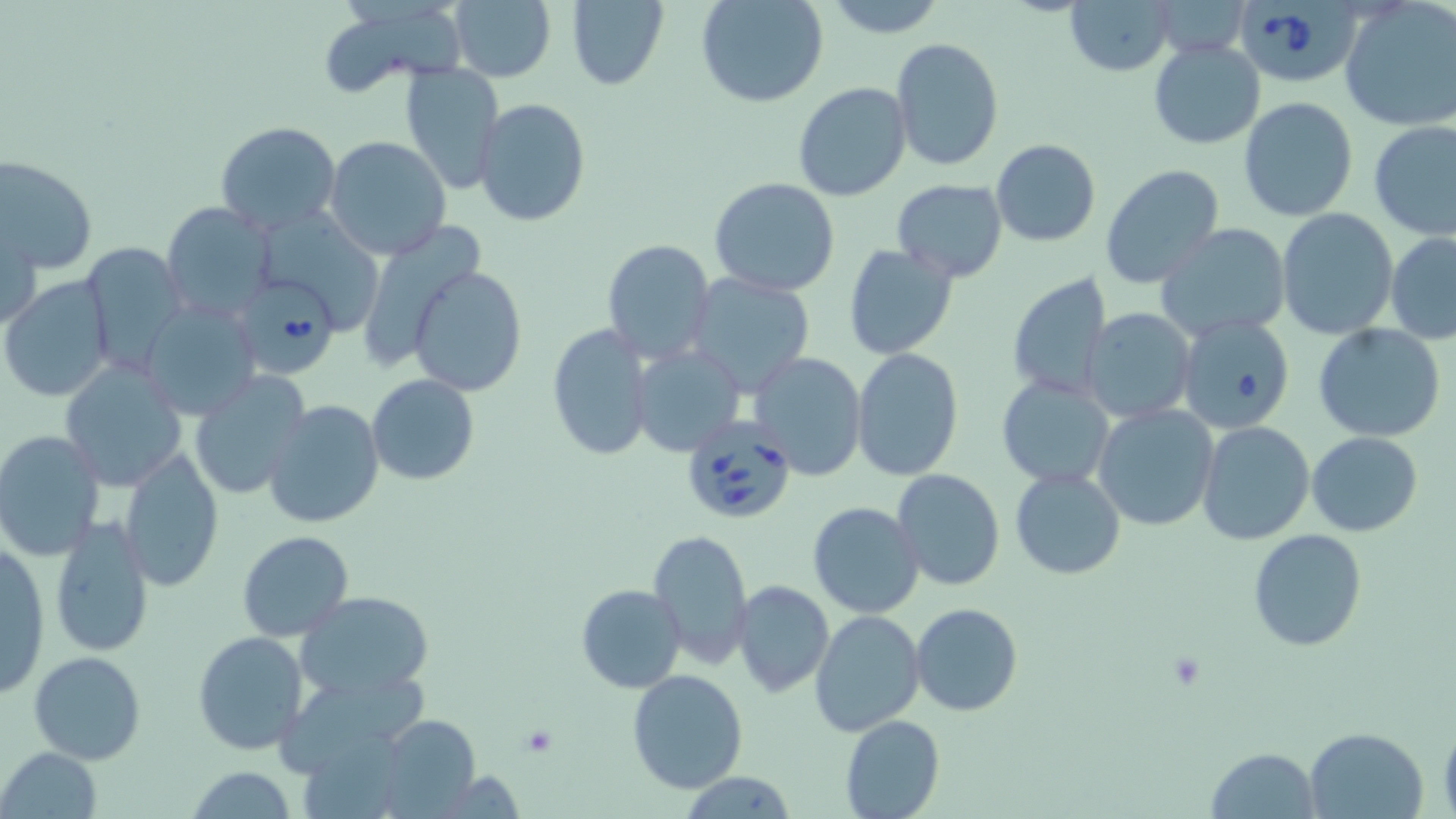 Approximate bounding boxes as (x1,y1)-(x2,y2) corner pairs in pixels. Platelet locations: (521,725)-(559,758). Uninfected red blood cell locations: (565,0)-(669,89), (696,0)-(828,108), (820,0)-(947,38), (1063,0)-(1174,77), (1340,1)-(1456,131), (448,2)-(556,82), (312,6)-(463,98), (891,37)-(1004,173), (1149,40)-(1264,150), (399,65)-(503,192), (793,82)-(911,201), (1238,96)-(1360,223), (475,98)-(590,227), (1368,120)-(1455,239), (215,122)-(343,234), (325,135)-(451,260), (991,139)-(1100,247), (0,155)-(99,275), (1099,162)-(1226,290), (709,176)-(841,297), (892,178)-(1008,282), (161,201)-(280,322), (1276,208)-(1398,339), (262,210)-(384,326), (2,215)-(41,335), (1156,223)-(1291,341), (365,224)-(485,354), (1386,231)-(1456,344), (603,238)-(716,364), (78,242)-(188,375), (843,243)-(960,362), (616,245)-(735,450), (409,263)-(527,397), (1005,271)-(1113,402), (685,272)-(815,395), (2,275)-(114,402), (140,297)-(260,419), (1082,308)-(1196,422), (1177,314)-(1296,434), (546,322)-(654,462), (1314,324)-(1446,442), (630,344)-(746,456), (850,347)-(962,482), (750,351)-(867,481), (58,357)-(188,489), (189,371)-(310,500), (366,374)-(479,486), (996,376)-(1114,489), (262,399)-(384,528), (1094,404)-(1221,532), (1196,420)-(1315,545), (0,428)-(104,560), (1307,431)-(1424,536), (118,449)-(225,593), (1009,468)-(1125,581), (892,469)-(1005,591), (808,502)-(924,619), (48,513)-(156,658), (1248,527)-(1368,651), (650,528)-(752,668), (238,530)-(354,642), (1,543)-(52,700), (732,582)-(835,698), (576,583)-(686,694), (294,590)-(435,700), (910,603)-(1025,717), (809,610)-(924,736), (192,631)-(309,756), (29,651)-(146,765), (625,668)-(748,794), (374,714)-(481,814), (839,714)-(946,819), (1439,717)-(1456,819), (1304,727)-(1427,818), (1208,745)-(1320,817), (1,747)-(102,818), (182,767)-(298,819), (678,772)-(800,818). Babesia divergens-infected red blood cell locations: (1233,0)-(1358,85), (246,279)-(341,374), (682,416)-(796,524). Slide-level diagnosis: Babesia divergens. Image is 1456×819 pixels. May-Grünwald-Giemsa stain. Light microscopy. Thin blood film. 1000x magnification. Single field of view.